Name the parasite shown.
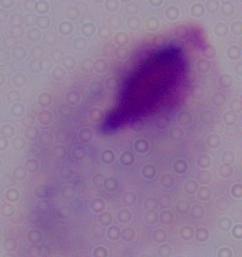

A trichomonad.

magnification = 1000x
modality = photomicrograph